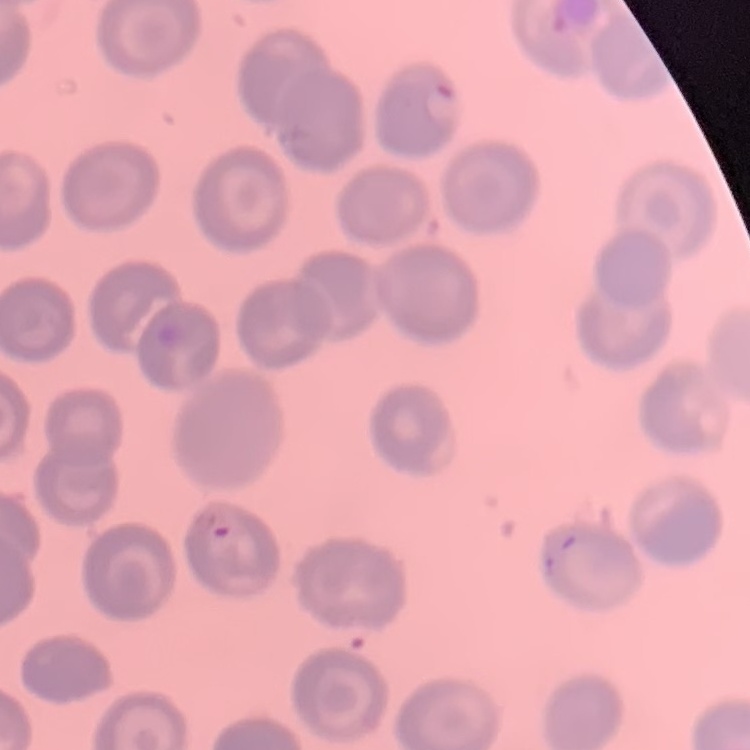

Summary:
  - Red blood cell morphology: no rouleaux formation
  - Image type: one tile cut from a larger photomicrograph
  - Preparation: thin blood smear
  - Stain: Field's or Giemsa